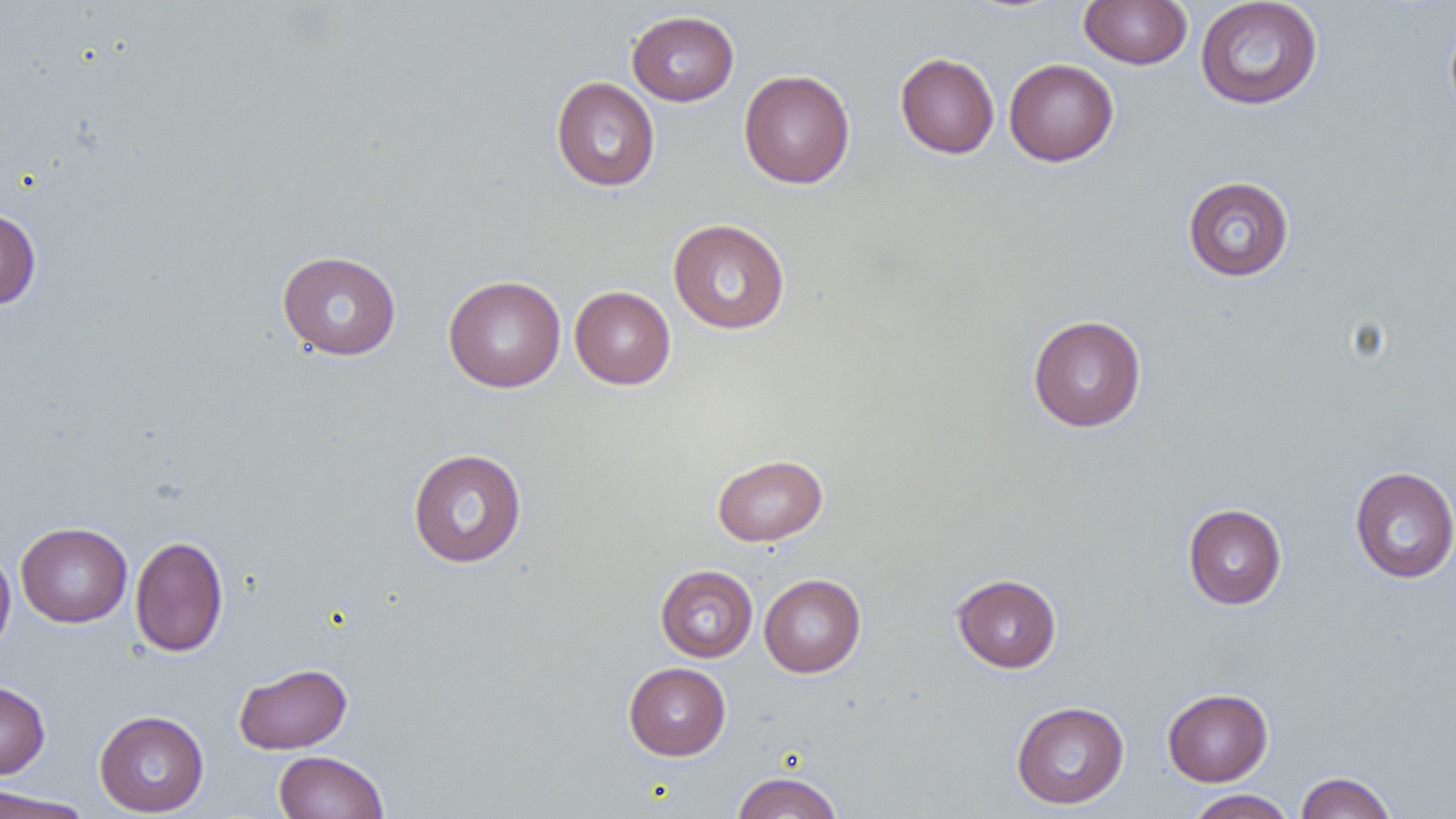

Summary:
  - Coordinate format: approximate bounding boxes as (x1,y1)-(x2,y2) corner pairs in pixels
  - Uninfected red blood cell locations: (1079,0)-(1192,69), (1195,1)-(1323,110), (627,10)-(739,106), (1445,12)-(1456,123), (895,52)-(999,159), (1004,58)-(1119,166), (738,70)-(855,188), (551,76)-(660,192), (1183,176)-(1295,281), (0,207)-(41,310), (668,218)-(791,334), (277,250)-(401,360), (443,275)-(566,392), (570,285)-(676,389), (1028,314)-(1146,432), (408,448)-(527,568), (712,453)-(828,546), (1349,466)-(1456,583), (1183,503)-(1287,609), (16,522)-(132,627), (130,535)-(229,657), (0,546)-(16,657), (655,565)-(757,662), (951,573)-(1062,673), (759,574)-(866,677), (234,662)-(352,754), (623,662)-(731,760), (0,680)-(50,779), (1162,687)-(1273,786), (1011,701)-(1130,809), (94,710)-(209,816), (273,751)-(389,819), (731,771)-(843,819), (1295,771)-(1398,819), (0,788)-(95,819), (1184,789)-(1298,818)
  - Slide-level diagnosis: negative for blood parasites
  - Image size: 1456×819 pixels
  - Modality: light microscopy
  - Magnification: 1000x
  - Preparation: thin blood film
  - Field of view: single